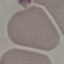

Summary:
  - Result: no malaria parasites detected
  - Stain: Giemsa
  - Capture: smartphone camera at the microscope eyepiece
  - Image type: automatically extracted cell patch, resized to 64 × 64 pixels
  - Preparation: thin smear